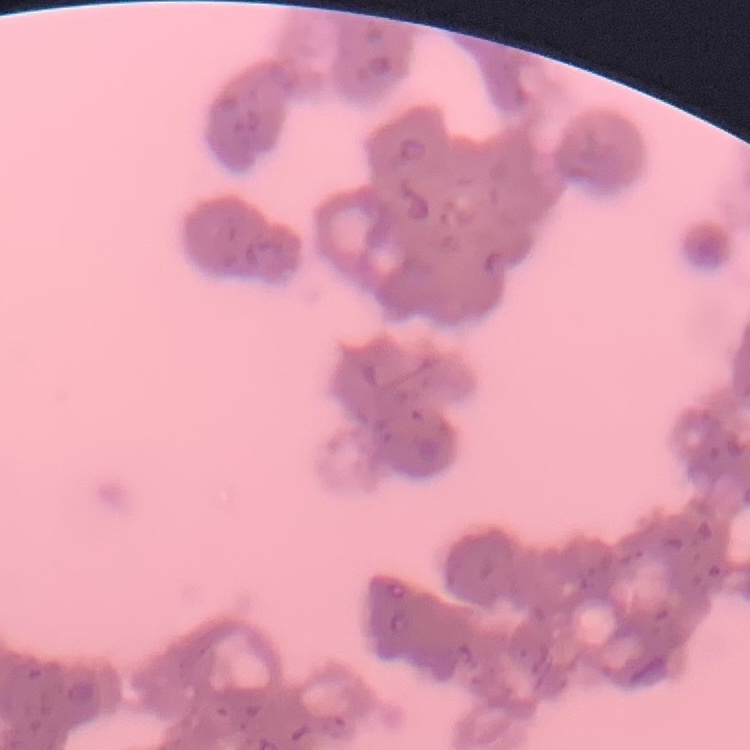

The erythrocytes exhibit rouleaux formation. Thin peripheral smear. Field's or Giemsa stain. One tile cut from a larger photomicrograph.